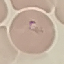

Summary:
  - Result: malaria parasites identified
  - Capture: smartphone through the microscope eyepiece
  - Preparation: thin smear
  - Image type: automatically extracted cell patch, resized to 64 × 64 pixels
  - Stain: Giemsa